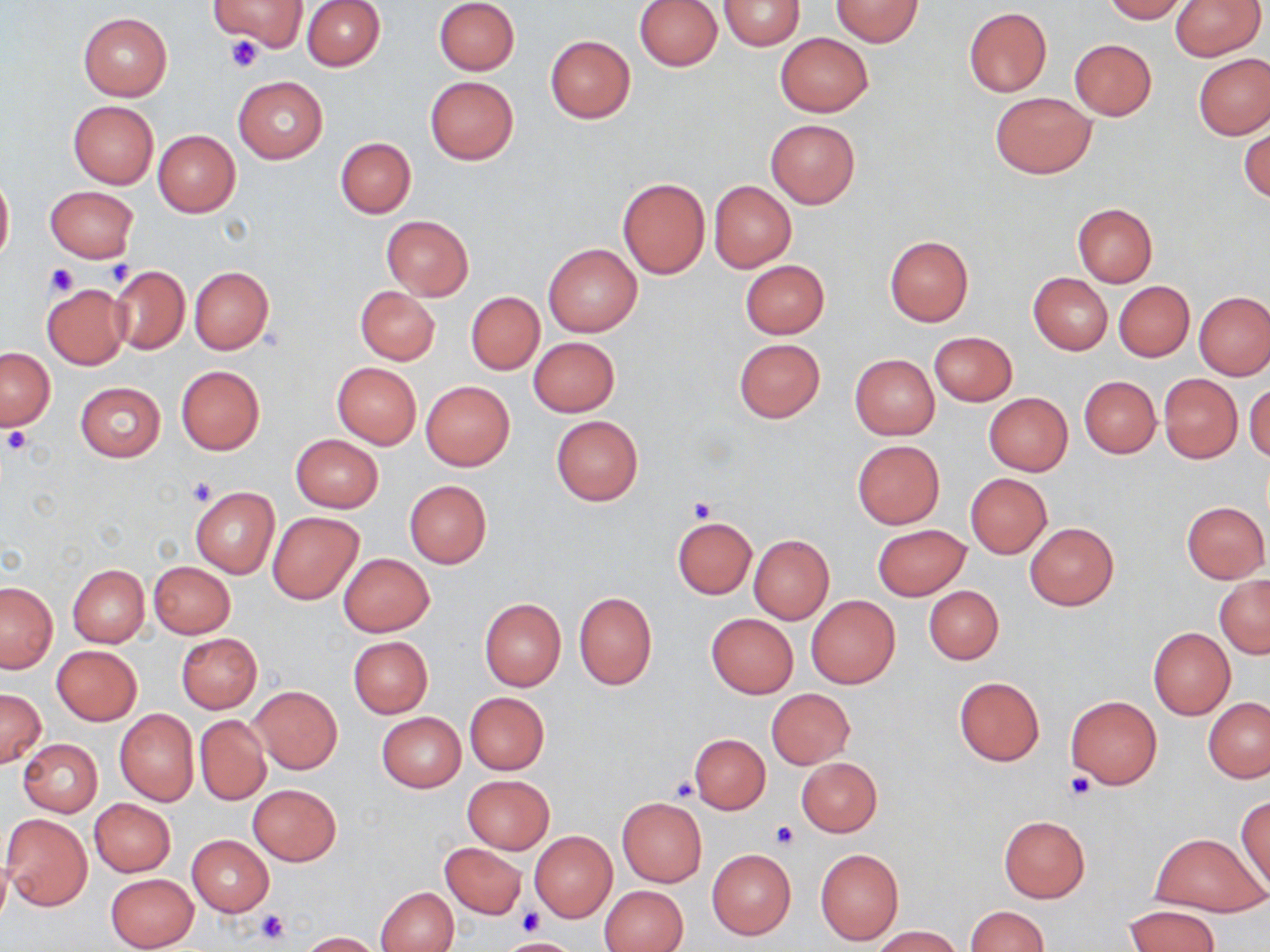
slide-level diagnosis = negative for blood parasites
platelet locations = approximate bounding boxes as (x1,y1)-(x2,y2) corner pairs in pixels: (225,36)-(262,73), (103,260)-(135,288), (44,264)-(79,297), (1,425)-(33,457), (187,476)-(218,507), (688,498)-(716,523), (1065,773)-(1096,801), (670,778)-(702,802), (769,821)-(798,850), (255,907)-(291,946), (517,907)-(541,934)
modality = light microscopy
magnification = 1000x
field of view = single
uninfected red blood cell locations = approximate bounding boxes as (x1,y1)-(x2,y2) corner pairs in pixels: (211,0)-(308,51), (302,0)-(385,70), (435,0)-(520,75), (719,0)-(805,49), (830,0)-(923,47), (1103,0)-(1188,23), (1169,0)-(1265,61), (636,1)-(721,70), (963,7)-(1052,97), (77,13)-(172,100), (775,32)-(873,117), (545,34)-(635,123), (1070,39)-(1156,119), (1194,54)-(1270,139), (233,76)-(328,163), (425,76)-(518,164), (989,92)-(1096,178), (68,100)-(158,188), (766,119)-(860,208), (1240,126)-(1269,203), (152,130)-(240,217), (335,137)-(415,218), (0,170)-(13,269), (616,176)-(711,279), (709,181)-(796,272), (45,186)-(137,262), (1072,203)-(1158,287), (381,215)-(473,300), (885,236)-(972,326), (543,243)-(642,336), (740,260)-(829,338), (107,264)-(190,356), (189,266)-(273,353), (1028,273)-(1112,354), (1114,281)-(1194,361), (41,282)-(129,370), (354,286)-(440,364), (1194,291)-(1269,380), (466,293)-(544,375), (929,331)-(1017,406), (528,337)-(620,417), (733,338)-(826,422), (1,348)-(54,430), (849,354)-(939,439), (332,362)-(421,448), (176,366)-(265,454), (1159,374)-(1242,463), (1079,375)-(1161,458), (1245,380)-(1270,463), (420,381)-(516,471), (75,382)-(165,461), (983,393)-(1073,475), (551,416)-(643,505), (291,434)-(383,512), (852,440)-(945,528), (964,473)-(1053,558), (404,480)-(491,568), (189,487)-(279,578), (1181,501)-(1269,582), (268,512)-(363,604), (672,516)-(756,599), (1025,522)-(1119,610), (872,524)-(970,600), (749,535)-(834,624), (337,552)-(435,637), (148,561)-(236,638), (67,564)-(149,646), (1214,575)-(1270,658), (0,581)-(57,673), (924,585)-(1004,664), (573,591)-(657,689), (806,594)-(901,689), (479,599)-(565,691), (706,613)-(798,698), (1147,627)-(1236,720), (177,633)-(263,713), (348,636)-(433,718), (52,645)-(141,725), (953,676)-(1044,767), (249,686)-(342,773), (0,688)-(45,769), (767,689)-(855,768), (464,693)-(550,774), (1066,695)-(1162,789), (1203,697)-(1270,782), (115,709)-(198,805), (377,712)-(465,792), (194,717)-(270,804), (689,734)-(771,814), (18,739)-(103,816), (796,758)-(882,837), (463,775)-(554,854), (248,784)-(341,865), (1236,795)-(1270,895), (89,798)-(175,877), (617,798)-(707,886), (2,813)-(92,910), (999,817)-(1090,902), (529,831)-(617,922), (1150,833)-(1265,917), (186,836)-(274,916), (439,843)-(525,919), (707,849)-(795,939), (815,849)-(904,945), (105,872)-(200,952), (600,886)-(688,952), (377,887)-(457,952), (1123,904)-(1221,952), (967,906)-(1049,952), (872,926)-(963,951), (299,931)-(382,951), (502,937)-(577,951)
preparation = thin blood film
stain = May-Grünwald-Giemsa
image size = 1270×952 pixels